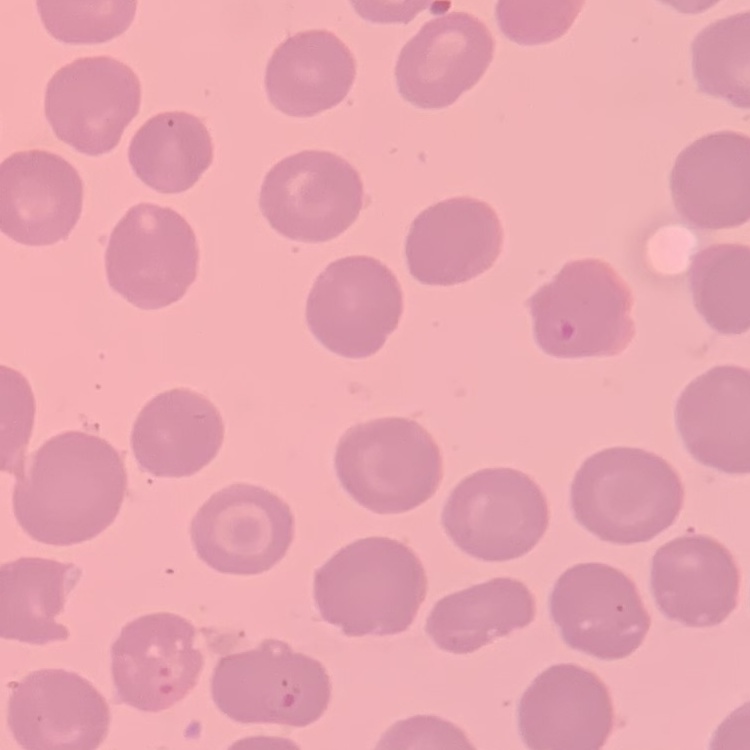 The erythrocytes show no rouleaux formation. Thin peripheral smear. Field's or Giemsa stain. One tile cut from a larger photomicrograph.